Name the cell type shown.
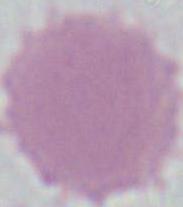
This is an erythrocyte.

1000x magnification. Photomicrograph.